Classify this cell by malaria status.
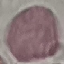
Uninfected.

Summary:
  - Preparation: thin blood film
  - Capture: smartphone camera at the microscope eyepiece
  - Image type: automatically extracted cell patch, resized to 64 × 64 pixels
  - Stain: Giemsa